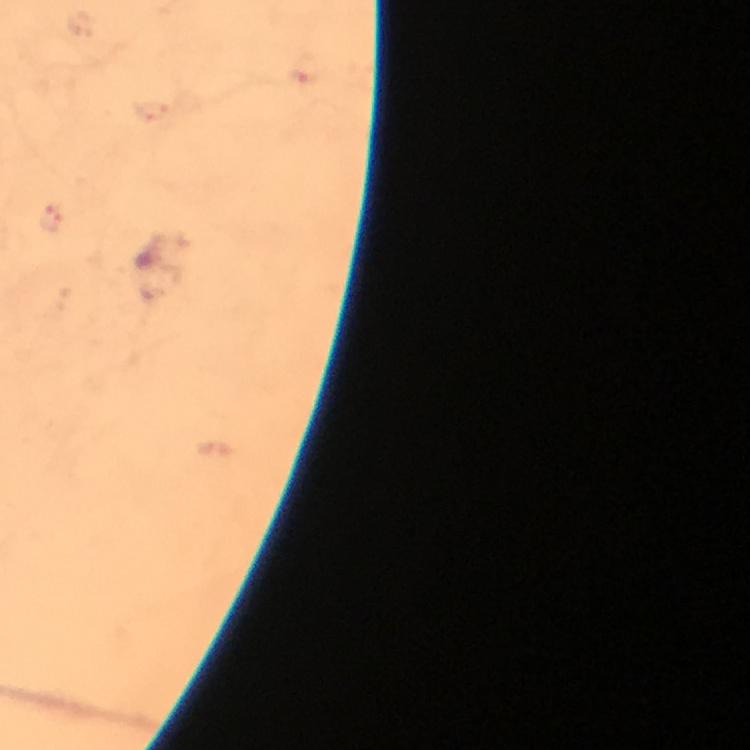

Approximate object centers, in pixels from the top-left corner. Plasmodium parasite locations: (x=54, y=220). Photographed through the microscope with a smartphone camera. At 100x magnification. Thick smear. From a malaria diagnostic workup. Giemsa-stained preparation. Immersion oil was used. Image is 750×750 pixels. A crop from one field of view.